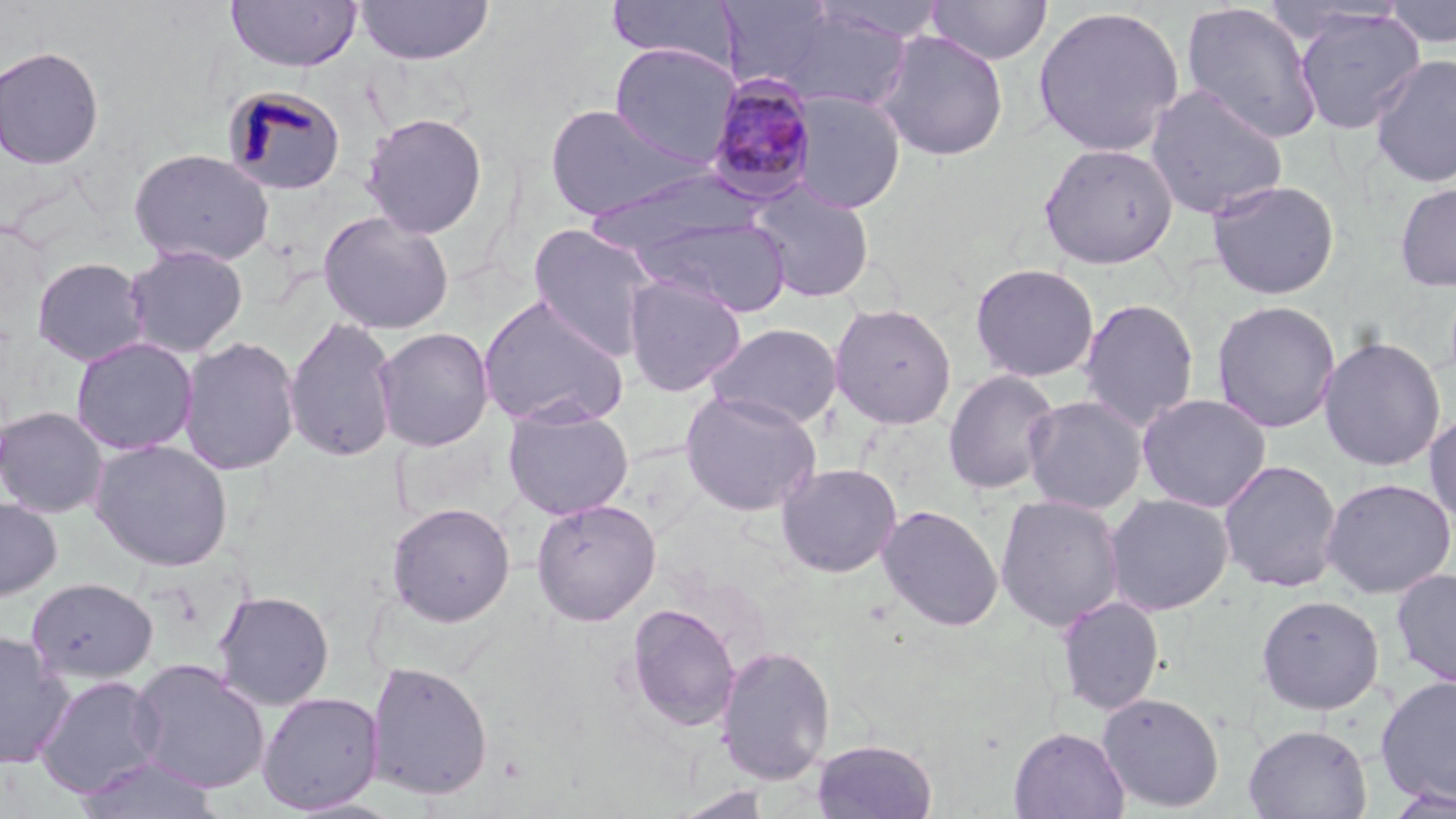

slide-level diagnosis = Plasmodium malariae
field of view = one of a larger specimen
modality = light microscopy
magnification = 1000x
stain = May-Grünwald-Giemsa
Plasmodium malariae-infected red blood cell locations = approximate bounding boxes as [x1, y1, x2, y2] in pixels: [701, 73, 820, 205]
uninfected red blood cell locations = approximate bounding boxes as [x1, y1, x2, y2] in pixels: [225, 0, 362, 72], [606, 0, 741, 69], [926, 0, 1053, 65], [1382, 0, 1456, 48], [353, 1, 494, 65], [1181, 2, 1324, 145], [758, 5, 920, 111], [1032, 6, 1185, 158], [1292, 6, 1425, 135], [875, 30, 1009, 161], [609, 42, 741, 166], [0, 45, 104, 170], [1369, 53, 1456, 188], [222, 84, 348, 197], [1144, 84, 1289, 220], [790, 92, 906, 214], [544, 103, 707, 220], [361, 112, 489, 239], [1038, 142, 1178, 269], [128, 148, 274, 268], [581, 168, 762, 256], [1206, 179, 1340, 300], [748, 180, 875, 304], [1395, 182, 1456, 292], [317, 210, 455, 335], [638, 215, 791, 317], [528, 223, 659, 361], [124, 244, 248, 358], [31, 256, 150, 366], [970, 262, 1099, 382], [623, 275, 746, 397], [477, 294, 629, 429], [1078, 298, 1199, 432], [1211, 300, 1341, 434], [829, 302, 957, 429], [283, 315, 400, 463], [706, 322, 843, 430], [373, 326, 495, 452], [177, 335, 302, 476], [1318, 336, 1447, 472], [69, 337, 199, 456], [942, 369, 1061, 495], [679, 388, 822, 516], [1136, 392, 1272, 513], [1022, 394, 1148, 514], [502, 404, 633, 520], [0, 406, 109, 518], [1423, 408, 1456, 528], [89, 439, 234, 571], [1218, 458, 1343, 593], [776, 462, 902, 578], [1320, 477, 1456, 598], [1104, 493, 1234, 616], [994, 494, 1125, 631], [0, 496, 62, 602], [530, 498, 661, 626], [386, 502, 516, 627], [877, 505, 1004, 632], [1391, 568, 1456, 689], [27, 577, 158, 685], [212, 589, 335, 711], [1255, 594, 1384, 715], [1055, 596, 1165, 715], [625, 602, 741, 732], [0, 631, 74, 767], [715, 644, 836, 785], [129, 658, 270, 794], [365, 660, 494, 802], [34, 675, 165, 798], [1374, 675, 1456, 808], [257, 690, 385, 814], [1097, 692, 1226, 812], [1243, 724, 1372, 819], [1008, 727, 1130, 818], [811, 738, 938, 819], [75, 753, 222, 818], [669, 787, 775, 818], [1381, 787, 1456, 818]
image size = 1456×819 pixels
preparation = thin blood film